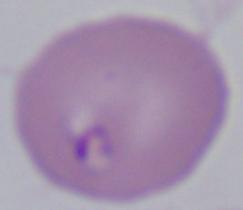
Summary:
  - Identification: Babesia
  - Magnification: 1000x
  - Modality: photomicrograph